Report the malaria status of this cell.
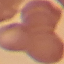

It is uninfected.

Acquired by smartphone through the microscope eyepiece. Thin smear of blood. Cell patch, automatically extracted from a larger field of view and resized to 64 × 64 pixels. Giemsa stain.